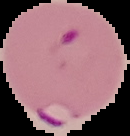

image size = 130×136 pixels
preparation = thin blood smear
malaria status = parasitized
image type = segmented cell region with the area outside set to black